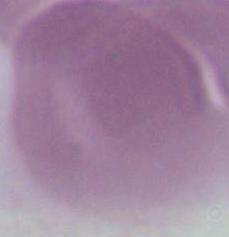

Summary:
  - Identification: red blood cell
  - Magnification: 1000x
  - Modality: micrograph